Assess this cell for malaria.
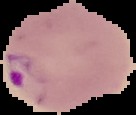

Parasitized.

Summary:
  - Image type: cell region segmented out of the field of view; surrounding area masked to black
  - Image size: 136×115 pixels
  - Preparation: thin blood film